State which parasite is depicted.
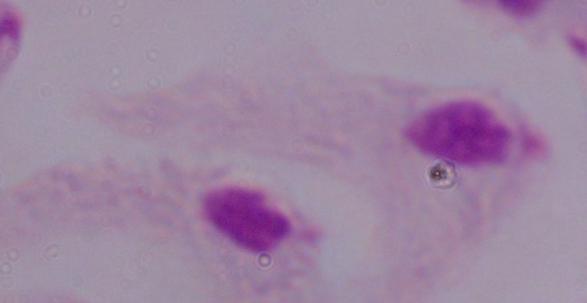
This is a trichomonad.

Summary:
  - Magnification: 1000x
  - Modality: micrograph